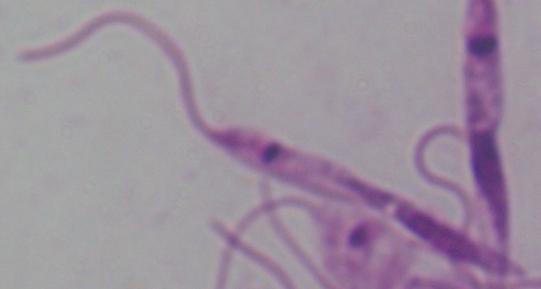

1000x magnification. A Leishmania parasite is seen. Micrograph.